Assess this cell for malaria.
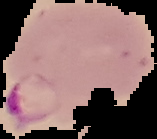
Parasitized.

image type = segmented cell region with the area outside set to black
preparation = thin blood smear
image size = 157×139 pixels